Locate every malaria parasite.
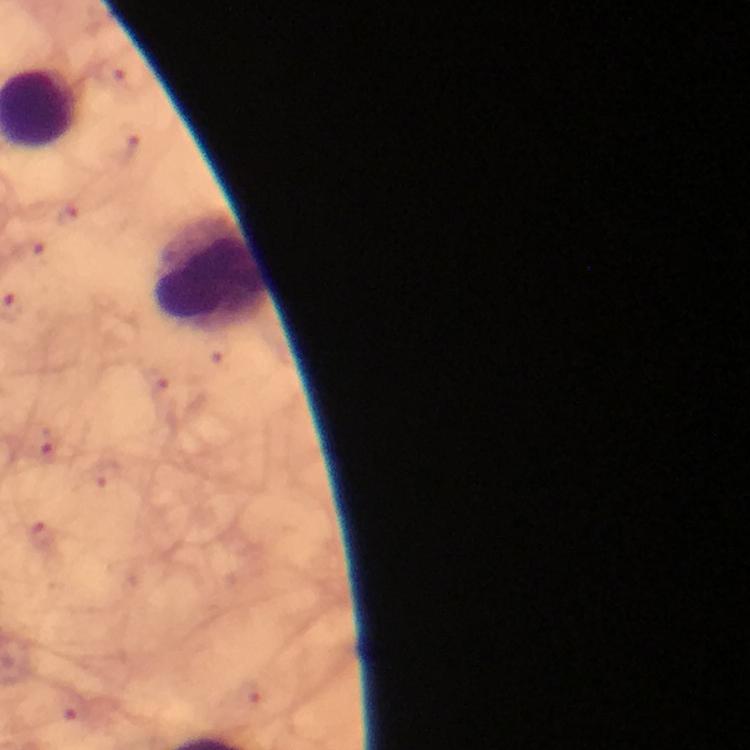

No malaria parasites seen.

preparation: thick smear
immersion_oil: applied
image_size: 750×750 pixels
cropped_from: one field of view
leukocyte_locations: 'approximate centers as [x, y] in pixels: [207, 270]'
magnification: 100x
stain: Giemsa
capture: smartphone mounted on the microscope
context: from a malaria diagnostic workup